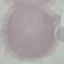

{
  "result": "no malaria parasites seen",
  "capture": "smartphone camera at the microscope eyepiece",
  "image_type": "automatically extracted cell patch, resized to 64 × 64 pixels",
  "stain": "Giemsa",
  "preparation": "thin smear"
}